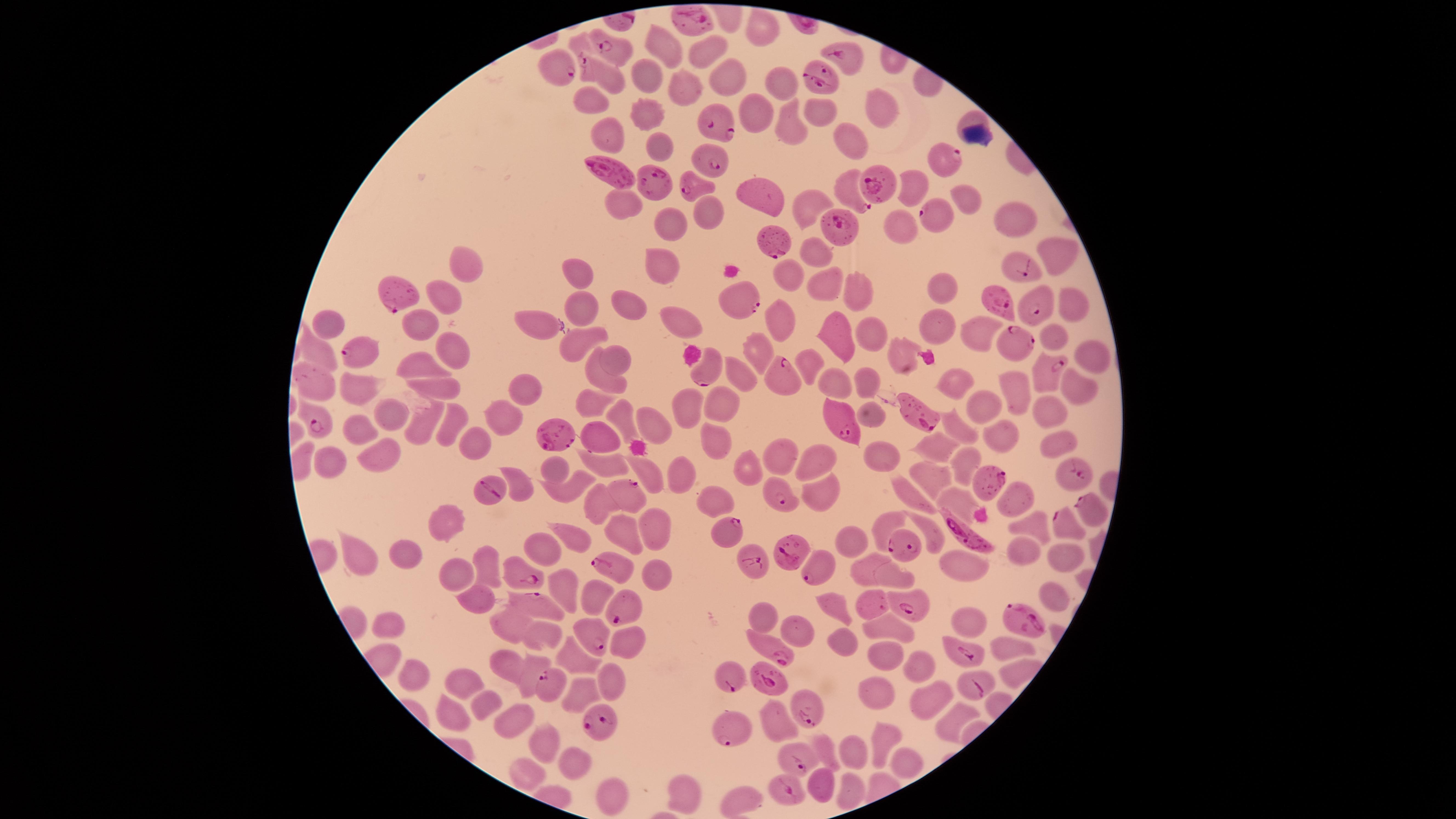
Approximate marker points, in pixels from the top-left corner.
Summary:
  - Parasitized RBCs: (x=699, y=22), (x=616, y=47), (x=844, y=54), (x=564, y=66), (x=593, y=68), (x=823, y=74), (x=720, y=120), (x=947, y=155), (x=713, y=162), (x=616, y=178), (x=696, y=181), (x=880, y=182), (x=658, y=185), (x=853, y=189), (x=941, y=210), (x=837, y=226), (x=774, y=239), (x=1021, y=271), (x=393, y=299), (x=737, y=299), (x=1002, y=306), (x=1040, y=306), (x=1018, y=346), (x=355, y=357), (x=1047, y=369), (x=708, y=371), (x=788, y=383), (x=914, y=410), (x=316, y=423), (x=838, y=428), (x=556, y=430), (x=1071, y=470), (x=990, y=481), (x=488, y=486), (x=776, y=489), (x=618, y=490), (x=1089, y=507), (x=1064, y=524), (x=963, y=528), (x=728, y=530), (x=903, y=545), (x=790, y=555), (x=755, y=561), (x=609, y=563), (x=820, y=571), (x=528, y=578), (x=873, y=602), (x=910, y=602), (x=540, y=603), (x=618, y=610), (x=1023, y=616), (x=593, y=641), (x=965, y=652), (x=774, y=654), (x=729, y=679), (x=771, y=680), (x=976, y=682), (x=551, y=688), (x=802, y=708), (x=599, y=725), (x=729, y=732), (x=794, y=760), (x=784, y=789)
  - Uninfected RBCs: (x=765, y=25), (x=580, y=42), (x=704, y=43), (x=665, y=46), (x=724, y=74), (x=650, y=76), (x=776, y=78), (x=688, y=87), (x=588, y=98), (x=880, y=108), (x=818, y=109), (x=648, y=110), (x=759, y=115), (x=787, y=120), (x=968, y=120), (x=602, y=127), (x=842, y=133), (x=660, y=144), (x=913, y=190), (x=759, y=196), (x=968, y=196), (x=806, y=198), (x=627, y=205), (x=706, y=211), (x=1011, y=214), (x=675, y=221), (x=896, y=223), (x=1058, y=250), (x=813, y=254), (x=466, y=260), (x=662, y=263), (x=788, y=269), (x=578, y=270), (x=816, y=281), (x=936, y=284), (x=853, y=285), (x=435, y=296), (x=1075, y=300), (x=581, y=302), (x=627, y=304), (x=778, y=313), (x=683, y=317), (x=420, y=323), (x=336, y=325), (x=542, y=325), (x=938, y=325), (x=875, y=330), (x=978, y=334), (x=841, y=335), (x=1051, y=336), (x=572, y=339), (x=316, y=345), (x=452, y=350), (x=901, y=353), (x=1093, y=353), (x=754, y=354), (x=614, y=355), (x=811, y=360), (x=422, y=366), (x=310, y=372), (x=596, y=374), (x=742, y=374), (x=871, y=379), (x=950, y=381), (x=836, y=383), (x=1075, y=384), (x=520, y=387), (x=352, y=389), (x=1014, y=389), (x=442, y=390), (x=594, y=400), (x=978, y=402), (x=684, y=404), (x=723, y=404), (x=389, y=408), (x=1049, y=408), (x=869, y=410), (x=506, y=415), (x=625, y=416), (x=422, y=420), (x=652, y=422), (x=950, y=422), (x=444, y=423), (x=357, y=426), (x=595, y=432), (x=713, y=439), (x=1005, y=440), (x=475, y=441), (x=1056, y=443), (x=935, y=446), (x=377, y=454), (x=781, y=455), (x=811, y=457), (x=331, y=458), (x=602, y=459), (x=961, y=462), (x=747, y=465), (x=551, y=467), (x=643, y=471), (x=685, y=476), (x=933, y=477), (x=564, y=491), (x=819, y=491), (x=911, y=494), (x=716, y=498), (x=956, y=498), (x=1011, y=498), (x=587, y=502), (x=1027, y=523), (x=450, y=524), (x=888, y=525), (x=928, y=528), (x=617, y=529), (x=651, y=529), (x=575, y=534), (x=855, y=540), (x=546, y=549), (x=1021, y=552), (x=412, y=555), (x=1066, y=556), (x=362, y=557), (x=961, y=560), (x=487, y=566), (x=863, y=570), (x=459, y=575), (x=656, y=575), (x=893, y=577), (x=564, y=583), (x=1056, y=593), (x=484, y=595), (x=589, y=598), (x=832, y=605), (x=763, y=619), (x=970, y=622), (x=390, y=623), (x=511, y=626), (x=885, y=626), (x=801, y=631), (x=545, y=635), (x=837, y=642), (x=631, y=643), (x=1005, y=644), (x=885, y=649), (x=579, y=660), (x=511, y=661), (x=916, y=663), (x=1019, y=670), (x=420, y=675), (x=610, y=678), (x=527, y=683), (x=459, y=685), (x=873, y=692), (x=584, y=693), (x=930, y=698), (x=485, y=701), (x=454, y=712), (x=953, y=721), (x=516, y=722), (x=776, y=723), (x=879, y=732), (x=546, y=742), (x=827, y=747), (x=849, y=754), (x=904, y=762), (x=581, y=763), (x=532, y=778), (x=824, y=784), (x=844, y=785), (x=680, y=792), (x=616, y=793), (x=742, y=798)
  - Image size: 1456×819 pixels
  - Capture: smartphone photograph through the microscope eyepiece
  - Presence: malaria parasites seen
  - Stain: Giemsa
  - Field of view: single
  - Species: Plasmodium falciparum
  - Visible region: circular
  - Preparation: thin smear of blood